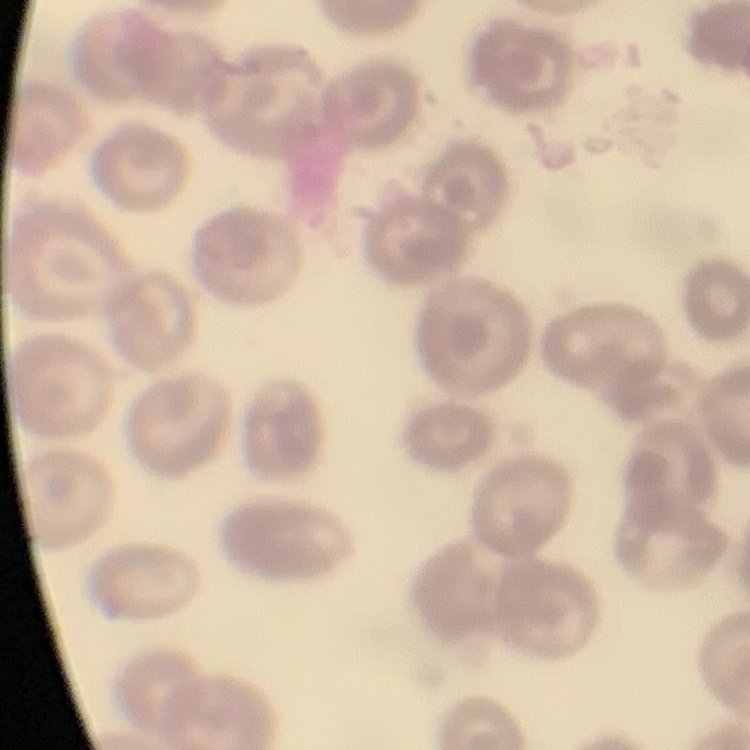

Summary:
  - Red blood cell morphology: no rouleaux formation
  - Image type: square crop of a larger photomicrograph
  - Preparation: thin peripheral smear
  - Stain: Field's or Giemsa